Draw a bounding box around every Plasmodium parasite, every leukocyte, and every artifact (stain precipitate or debris).
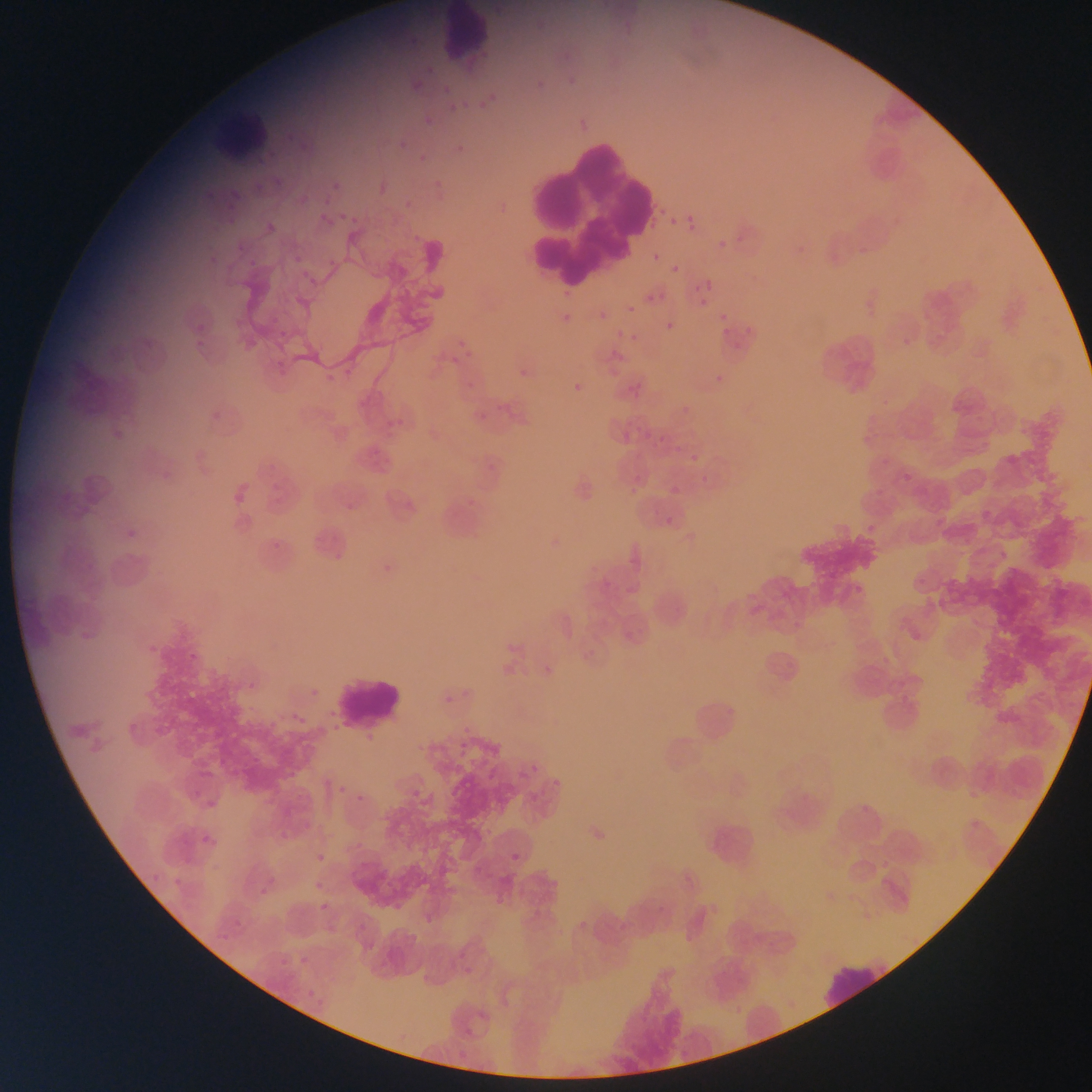
Approximate bounding boxes as [left, top, right, bottom] in pixels.
Plasmodium parasites: [534, 22, 545, 33], [560, 43, 579, 58], [425, 65, 438, 74], [561, 73, 576, 88], [533, 78, 542, 87], [412, 82, 420, 95], [437, 88, 453, 97], [475, 91, 501, 113], [446, 99, 469, 115], [425, 115, 437, 125], [297, 139, 311, 152], [392, 140, 407, 151], [452, 141, 469, 157], [415, 152, 432, 162], [333, 180, 349, 193], [431, 180, 443, 187], [226, 189, 241, 200], [401, 192, 420, 209], [322, 198, 335, 208], [335, 207, 359, 223], [222, 210, 238, 225], [683, 210, 696, 226], [317, 214, 337, 229], [670, 218, 678, 226], [263, 219, 282, 233], [685, 225, 694, 233], [411, 231, 422, 241], [714, 240, 722, 251], [230, 245, 250, 254], [204, 246, 228, 273], [244, 250, 265, 269], [293, 251, 305, 262], [653, 253, 662, 262], [322, 255, 338, 267], [670, 264, 680, 273], [293, 267, 311, 277], [307, 274, 325, 286], [703, 281, 714, 290], [556, 284, 570, 301], [693, 285, 701, 294], [646, 295, 654, 303], [698, 298, 707, 307], [627, 305, 635, 313], [597, 310, 603, 318], [718, 313, 726, 322], [556, 314, 569, 327], [266, 315, 285, 328], [612, 318, 630, 340], [193, 321, 209, 335], [666, 322, 675, 331], [723, 327, 730, 335], [622, 328, 640, 340], [279, 330, 289, 336], [189, 336, 212, 358], [731, 336, 742, 351], [452, 337, 470, 347], [142, 338, 154, 352], [465, 348, 473, 358], [449, 354, 456, 365], [272, 356, 285, 374], [516, 360, 530, 380], [339, 365, 353, 379], [325, 373, 331, 385], [714, 374, 722, 383], [469, 381, 477, 390], [574, 383, 582, 391], [629, 388, 638, 399], [677, 401, 687, 414], [208, 411, 220, 421], [477, 412, 487, 421], [380, 417, 390, 430], [381, 428, 395, 441], [622, 432, 631, 442], [655, 432, 664, 446], [367, 441, 388, 473], [687, 445, 706, 463], [677, 447, 689, 454], [487, 464, 495, 472], [700, 471, 710, 484], [904, 473, 913, 482], [670, 485, 681, 496], [629, 486, 638, 496], [269, 494, 282, 505], [464, 495, 480, 510], [345, 502, 354, 512], [982, 510, 991, 520], [666, 516, 675, 525], [127, 520, 141, 542], [269, 533, 290, 550], [333, 545, 348, 564], [625, 547, 647, 567], [382, 559, 394, 574], [597, 572, 612, 586], [499, 631, 523, 651], [620, 632, 631, 642], [184, 638, 207, 660], [579, 638, 605, 660], [149, 644, 159, 653], [541, 666, 554, 679], [246, 680, 256, 693], [307, 684, 322, 699], [439, 690, 458, 705], [264, 701, 295, 728], [244, 702, 259, 715], [288, 705, 315, 728], [721, 706, 742, 724], [362, 722, 381, 742], [454, 735, 470, 754], [523, 761, 543, 780], [404, 767, 432, 801], [550, 768, 570, 790], [331, 776, 352, 799], [521, 784, 548, 803], [202, 787, 221, 813], [354, 792, 369, 803], [200, 833, 217, 848], [506, 851, 520, 862], [317, 852, 326, 862], [142, 870, 162, 883], [169, 871, 191, 890], [256, 877, 276, 896], [315, 880, 324, 890], [320, 902, 330, 912], [227, 911, 243, 926], [577, 913, 596, 929], [217, 929, 232, 950], [295, 944, 311, 969], [276, 948, 290, 967], [302, 985, 318, 1004], [308, 993, 331, 1012], [478, 1009, 490, 1020], [465, 1028, 475, 1039] | approximate [x, y] pixel centers of objects too small to bound: [399, 419].
Leukocytes: [434, 0, 487, 57], [222, 112, 268, 160], [528, 141, 670, 279], [332, 673, 400, 732], [818, 958, 895, 1012].

Photographed through a microscope with a mobile-phone camera. Collected in Ghana. Image is 1092×1092 pixels. Single field of view. Thin blood smear.